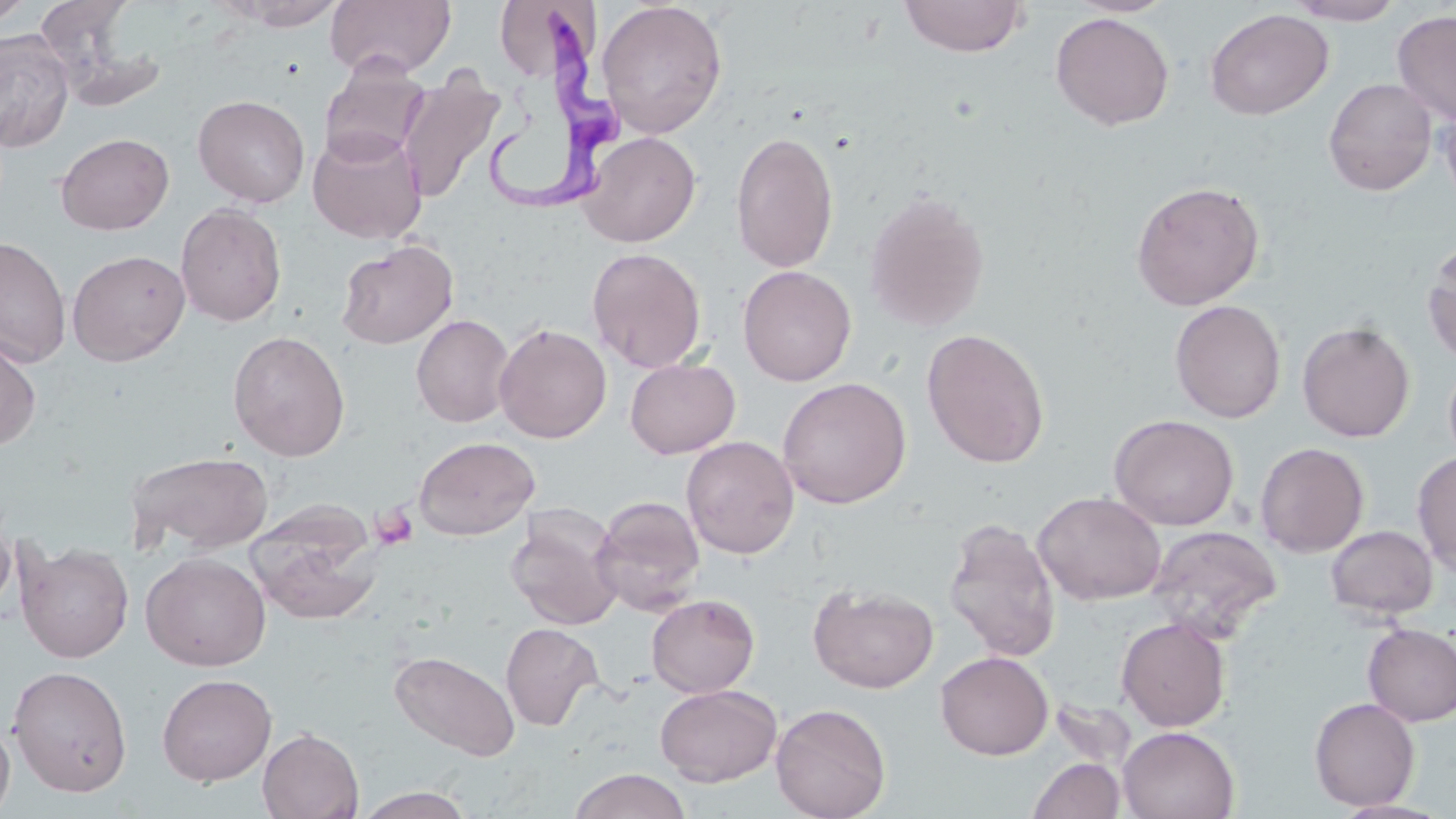

slide-level diagnosis = Trypanosoma brucei
image size = 1456×819 pixels
field of view = single
Trypanosoma brucei locations = approximate bounding boxes as named x1/y1/x2/y2 corners in pixels: (x1=480, y1=10, x2=630, y2=215)
uninfected red blood cell locations = approximate bounding boxes as named x1/y1/x2/y2 corners in pixels: (x1=1, y1=0, x2=33, y2=26), (x1=325, y1=0, x2=456, y2=80), (x1=497, y1=0, x2=597, y2=85), (x1=899, y1=0, x2=1029, y2=58), (x1=1286, y1=0, x2=1406, y2=25), (x1=33, y1=1, x2=139, y2=84), (x1=224, y1=1, x2=344, y2=29), (x1=596, y1=1, x2=728, y2=139), (x1=1205, y1=8, x2=1334, y2=120), (x1=1393, y1=9, x2=1456, y2=127), (x1=1050, y1=11, x2=1174, y2=131), (x1=0, y1=30, x2=75, y2=152), (x1=319, y1=58, x2=429, y2=166), (x1=397, y1=68, x2=505, y2=204), (x1=1323, y1=77, x2=1437, y2=196), (x1=193, y1=94, x2=310, y2=207), (x1=1437, y1=95, x2=1456, y2=213), (x1=308, y1=127, x2=428, y2=244), (x1=730, y1=129, x2=839, y2=273), (x1=578, y1=131, x2=701, y2=247), (x1=55, y1=133, x2=174, y2=235), (x1=1130, y1=180, x2=1265, y2=311), (x1=863, y1=189, x2=992, y2=333), (x1=175, y1=203, x2=287, y2=327), (x1=0, y1=236, x2=72, y2=369), (x1=1422, y1=236, x2=1456, y2=367), (x1=336, y1=240, x2=458, y2=349), (x1=587, y1=247, x2=707, y2=374), (x1=67, y1=249, x2=190, y2=366), (x1=738, y1=265, x2=856, y2=386), (x1=1170, y1=299, x2=1286, y2=423), (x1=411, y1=314, x2=515, y2=428), (x1=1297, y1=321, x2=1415, y2=443), (x1=494, y1=324, x2=612, y2=443), (x1=921, y1=327, x2=1050, y2=468), (x1=0, y1=330, x2=42, y2=451), (x1=227, y1=330, x2=350, y2=461), (x1=625, y1=357, x2=740, y2=459), (x1=1443, y1=357, x2=1456, y2=470), (x1=777, y1=376, x2=912, y2=509), (x1=1109, y1=413, x2=1239, y2=531), (x1=413, y1=435, x2=540, y2=540), (x1=681, y1=435, x2=800, y2=559), (x1=1254, y1=441, x2=1370, y2=557), (x1=126, y1=450, x2=274, y2=556), (x1=1412, y1=451, x2=1456, y2=576), (x1=1033, y1=491, x2=1166, y2=605), (x1=591, y1=495, x2=705, y2=615), (x1=0, y1=504, x2=16, y2=617), (x1=249, y1=504, x2=382, y2=625), (x1=506, y1=511, x2=623, y2=630), (x1=943, y1=517, x2=1061, y2=663), (x1=1145, y1=525, x2=1282, y2=642), (x1=1325, y1=525, x2=1438, y2=619), (x1=15, y1=539, x2=135, y2=663), (x1=140, y1=552, x2=271, y2=671), (x1=808, y1=583, x2=938, y2=693), (x1=646, y1=594, x2=760, y2=698), (x1=1116, y1=617, x2=1231, y2=731), (x1=500, y1=622, x2=603, y2=731), (x1=1362, y1=623, x2=1456, y2=726), (x1=389, y1=650, x2=521, y2=761), (x1=935, y1=651, x2=1053, y2=760), (x1=7, y1=665, x2=132, y2=798), (x1=156, y1=673, x2=277, y2=786), (x1=655, y1=684, x2=782, y2=786), (x1=1309, y1=696, x2=1420, y2=811), (x1=1049, y1=698, x2=1137, y2=777), (x1=770, y1=702, x2=892, y2=819), (x1=0, y1=718, x2=15, y2=818), (x1=1117, y1=726, x2=1239, y2=819), (x1=258, y1=727, x2=364, y2=819), (x1=1028, y1=757, x2=1126, y2=819), (x1=568, y1=768, x2=693, y2=819), (x1=354, y1=787, x2=476, y2=819), (x1=1330, y1=798, x2=1452, y2=819)
platelet locations = approximate bounding boxes as named x1/y1/x2/y2 corners in pixels: (x1=370, y1=504, x2=419, y2=551)
modality = optical microscopy
magnification = 1000x
preparation = thin blood film
stain = May-Grünwald-Giemsa